Give the extent of all Plasmodium falciparum-infected red blood cells.
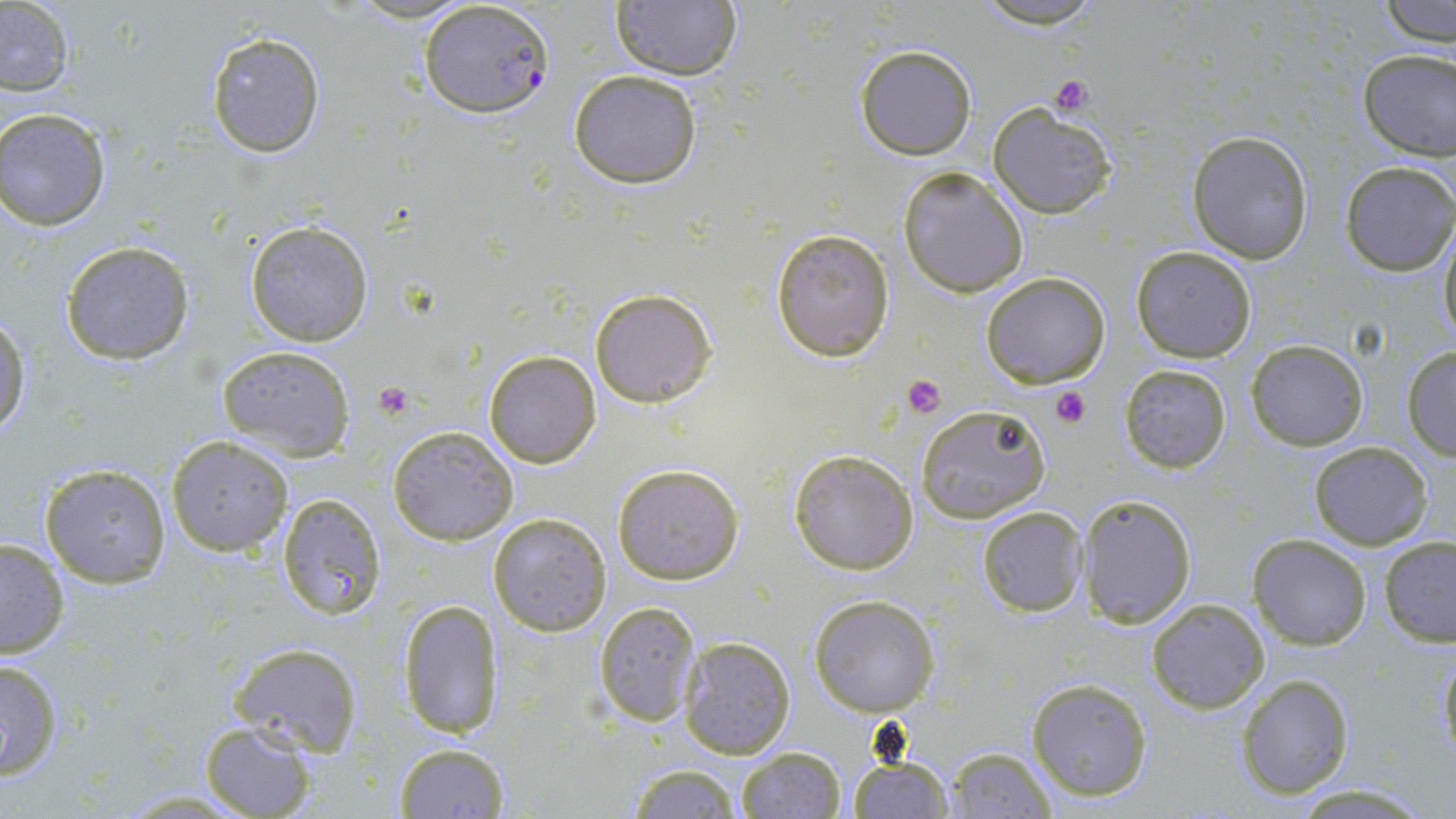
Approximate bounding boxes as [x1, y1, x2, y2] in pixels.
Plasmodium falciparum-infected red blood cells: [419, 0, 553, 119].

{
  "slide_level_diagnosis": "Plasmodium falciparum",
  "field_of_view": "single",
  "image_size": "1456×819 pixels",
  "uninfected_red_blood_cell_locations": "approximate bounding boxes as [x1, y1, x2, y2] in pixels: [609, 1, 744, 81], [1381, 1, 1456, 47], [968, 2, 1112, 29], [0, 3, 75, 95], [206, 31, 326, 157], [855, 44, 977, 161], [1356, 48, 1455, 160], [570, 70, 703, 188], [988, 101, 1118, 219], [0, 109, 113, 232], [1188, 130, 1313, 263], [1339, 162, 1455, 275], [898, 166, 1029, 297], [245, 220, 373, 347], [1437, 224, 1456, 345], [770, 229, 895, 362], [62, 240, 193, 364], [1131, 245, 1257, 363], [980, 272, 1112, 389], [590, 287, 718, 408], [0, 315, 30, 440], [1246, 338, 1368, 450], [217, 345, 354, 461], [1402, 346, 1456, 458], [483, 350, 601, 467], [1118, 362, 1232, 474], [198, 372, 336, 524], [915, 404, 1049, 523], [389, 425, 518, 545], [167, 436, 293, 556], [1309, 441, 1433, 550], [790, 449, 917, 574], [39, 461, 172, 588], [611, 462, 744, 586], [276, 492, 387, 620], [1078, 492, 1197, 626], [977, 506, 1087, 617], [490, 513, 611, 635], [1248, 534, 1372, 649], [1380, 537, 1456, 645], [0, 538, 71, 660], [809, 595, 939, 717], [399, 598, 505, 737], [1147, 598, 1270, 714], [593, 599, 702, 727], [678, 635, 796, 757], [229, 642, 362, 755], [1437, 645, 1456, 771], [0, 658, 64, 780], [1236, 674, 1356, 799], [1025, 678, 1152, 803], [201, 721, 317, 819], [393, 742, 509, 817], [735, 747, 846, 819], [945, 747, 1057, 818], [847, 755, 951, 817], [622, 765, 744, 817], [1290, 784, 1436, 817], [111, 788, 260, 817]",
  "modality": "light microscopy",
  "magnification": "1000x",
  "platelet_locations": "approximate bounding boxes as [x1, y1, x2, y2] in pixels: [1049, 76, 1093, 117], [900, 373, 947, 418], [375, 382, 415, 419], [1050, 384, 1092, 429]",
  "stain": "May-Grünwald-Giemsa",
  "preparation": "thin blood film"
}